Give the preparation type.
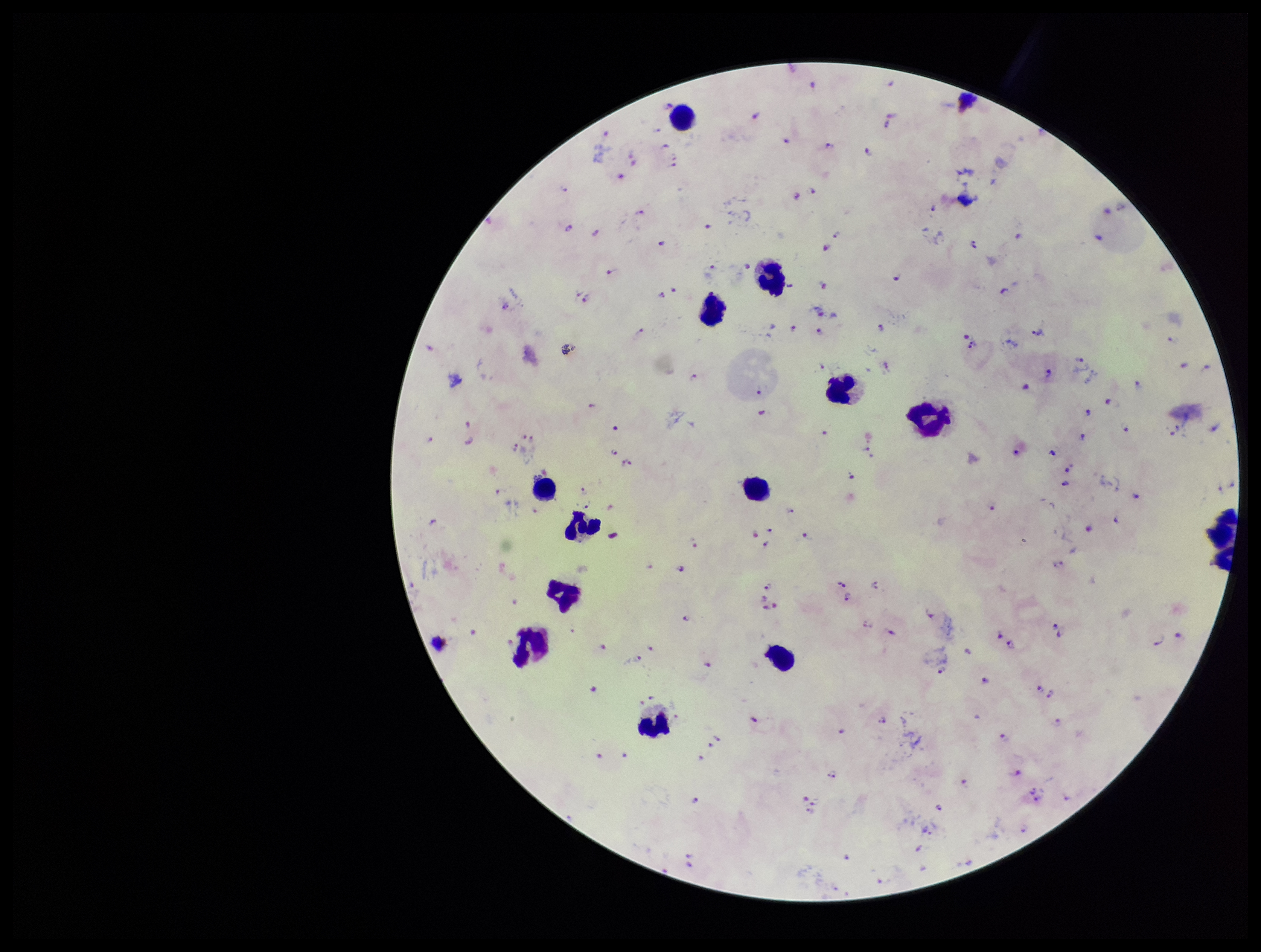

It is a thick blood smear.

Summary:
  - Species reported for this patient: Plasmodium falciparum
  - Leukocyte count: 13
  - Parasite count: 113
  - Capture: smartphone photograph through the microscope eyepiece
  - Plasmodium parasites: seen
  - Image size: 1261×952 pixels
  - Stain: Giemsa
  - Patient malaria status: infected
  - Field of view: single